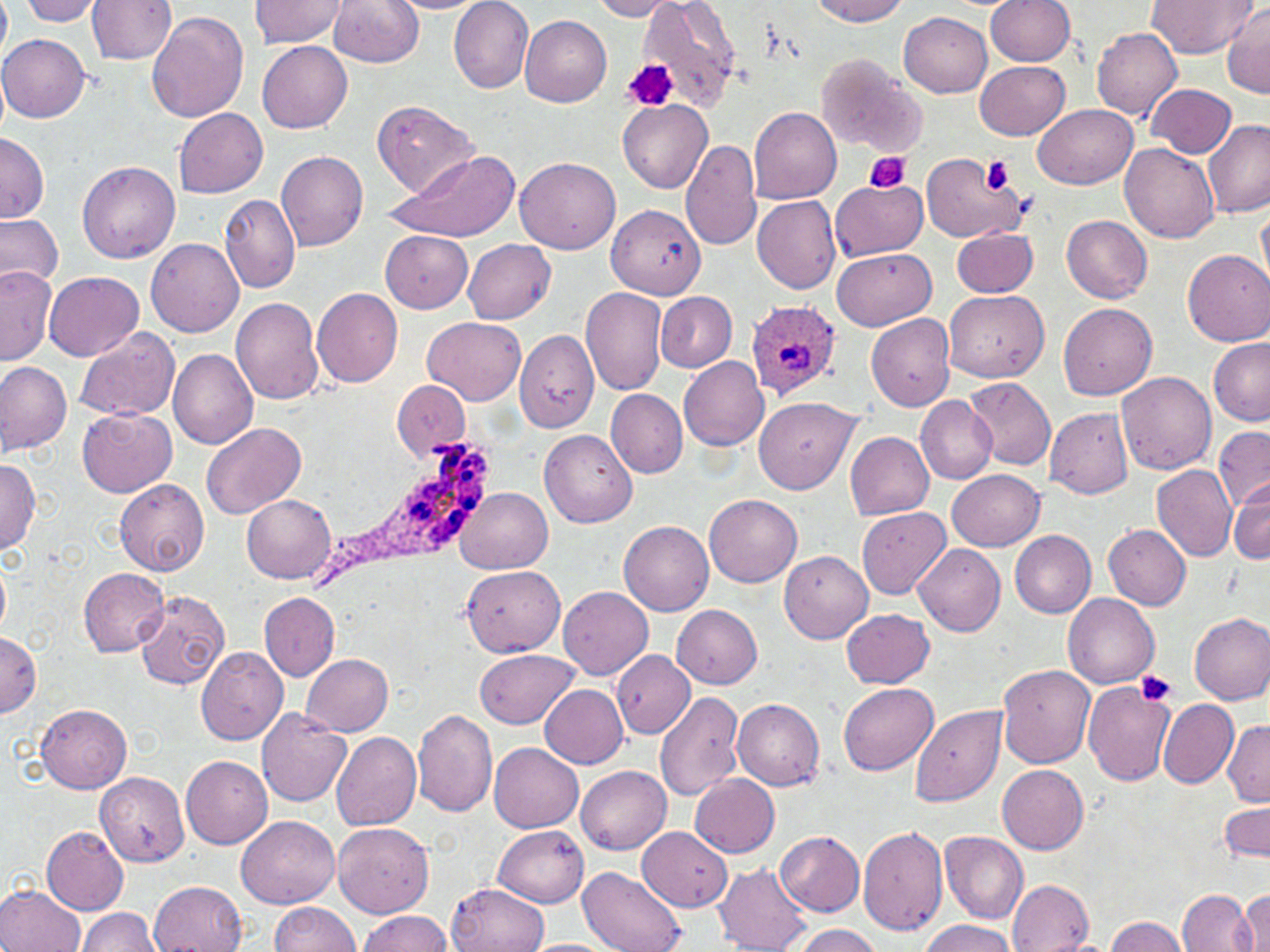

Approximate bounding boxes as (x1,y1)-(x2,y2) corner pairs in pixels. Uninfected red blood cell locations: (0,0)-(12,64), (18,0)-(105,25), (247,0)-(349,48), (329,0)-(423,67), (811,0)-(911,25), (1146,0)-(1255,58), (87,1)-(176,64), (384,1)-(493,14), (591,1)-(686,20), (638,1)-(742,109), (984,1)-(1075,65), (448,2)-(534,93), (1221,4)-(1270,99), (147,12)-(249,124), (900,12)-(992,97), (520,15)-(611,107), (1092,27)-(1183,119), (0,34)-(90,123), (258,41)-(352,133), (817,54)-(924,156), (975,61)-(1069,140), (1147,83)-(1236,158), (372,98)-(480,200), (618,100)-(712,193), (1033,104)-(1140,190), (748,106)-(843,204), (174,107)-(268,198), (1203,119)-(1269,216), (0,133)-(49,224), (681,139)-(762,252), (1120,143)-(1218,245), (388,149)-(517,241), (276,151)-(368,250), (921,152)-(1027,244), (514,155)-(620,252), (78,161)-(179,264), (831,177)-(927,259), (218,194)-(301,294), (753,195)-(842,293), (1256,202)-(1269,289), (606,204)-(705,298), (0,211)-(63,292), (1062,215)-(1153,303), (951,227)-(1039,297), (380,230)-(473,312), (146,238)-(244,338), (463,239)-(556,324), (832,248)-(936,330), (1183,249)-(1270,345), (0,265)-(56,365), (44,272)-(143,362), (580,286)-(669,396), (312,287)-(403,388), (944,289)-(1049,383), (657,291)-(736,372), (232,297)-(324,404), (1059,302)-(1158,400), (865,311)-(955,412), (421,317)-(525,406), (75,327)-(180,422), (515,330)-(600,434), (1207,338)-(1270,427), (168,348)-(258,451), (679,356)-(769,451), (0,362)-(72,454), (1116,371)-(1216,472), (965,377)-(1056,471), (391,380)-(471,461), (606,389)-(688,477), (915,395)-(998,484), (755,398)-(862,494), (77,407)-(176,497), (1045,409)-(1134,498), (200,423)-(305,519), (1213,425)-(1270,513), (540,430)-(637,528), (845,431)-(935,520), (0,458)-(41,553), (1152,465)-(1238,562), (946,468)-(1044,551), (1230,477)-(1270,564), (114,478)-(210,577), (456,488)-(553,574), (242,493)-(337,581), (705,494)-(803,587), (857,507)-(950,599), (619,520)-(715,615), (1104,525)-(1192,610), (1010,530)-(1096,617), (914,544)-(1006,637), (779,551)-(874,645), (0,557)-(11,635), (460,566)-(566,656), (79,567)-(170,656), (558,587)-(653,680), (134,589)-(229,689), (260,593)-(339,679), (1063,593)-(1160,688), (673,604)-(762,689), (843,608)-(935,689), (1188,612)-(1270,704), (0,632)-(40,717), (196,645)-(288,745), (477,649)-(579,729), (613,652)-(694,736), (299,653)-(393,735), (997,664)-(1095,770), (1083,681)-(1176,786), (838,683)-(939,775), (539,685)-(628,768), (655,690)-(746,801), (732,698)-(825,791), (1158,698)-(1238,788), (35,703)-(131,794), (911,706)-(1008,806), (257,708)-(354,807), (412,709)-(498,818), (1222,720)-(1270,808), (331,730)-(421,833), (489,743)-(584,831), (181,756)-(272,849), (576,766)-(671,853), (997,766)-(1088,853), (95,772)-(191,867), (691,775)-(780,858), (1219,799)-(1269,863), (235,814)-(340,909), (332,822)-(434,917), (39,823)-(129,916), (494,826)-(588,907), (637,826)-(732,911), (857,826)-(948,936), (775,830)-(865,915), (939,831)-(1028,924), (715,864)-(813,952), (577,866)-(686,952), (1008,878)-(1096,952), (149,880)-(245,951), (448,881)-(545,952), (0,883)-(85,952), (1178,889)-(1257,951), (1238,890)-(1270,951), (267,902)-(362,952), (77,908)-(162,952), (357,911)-(452,951), (1105,916)-(1191,952), (919,919)-(1016,952), (791,924)-(882,952), (520,939)-(621,952). Platelet locations: (619,58)-(677,113), (861,151)-(910,193), (981,157)-(1014,195), (1136,669)-(1177,706). Plasmodium ovale-infected red blood cell locations: (746,300)-(845,400), (314,436)-(494,591). Slide-level diagnosis: Plasmodium ovale. Thin blood smear. One field of a larger specimen. Captured at 1000x magnification. May-Grünwald-Giemsa stain. Light microscopy. Image is 1270×952 pixels.